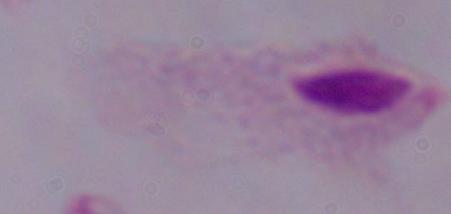

identification = trichomonad
magnification = 1000x
modality = photomicrograph